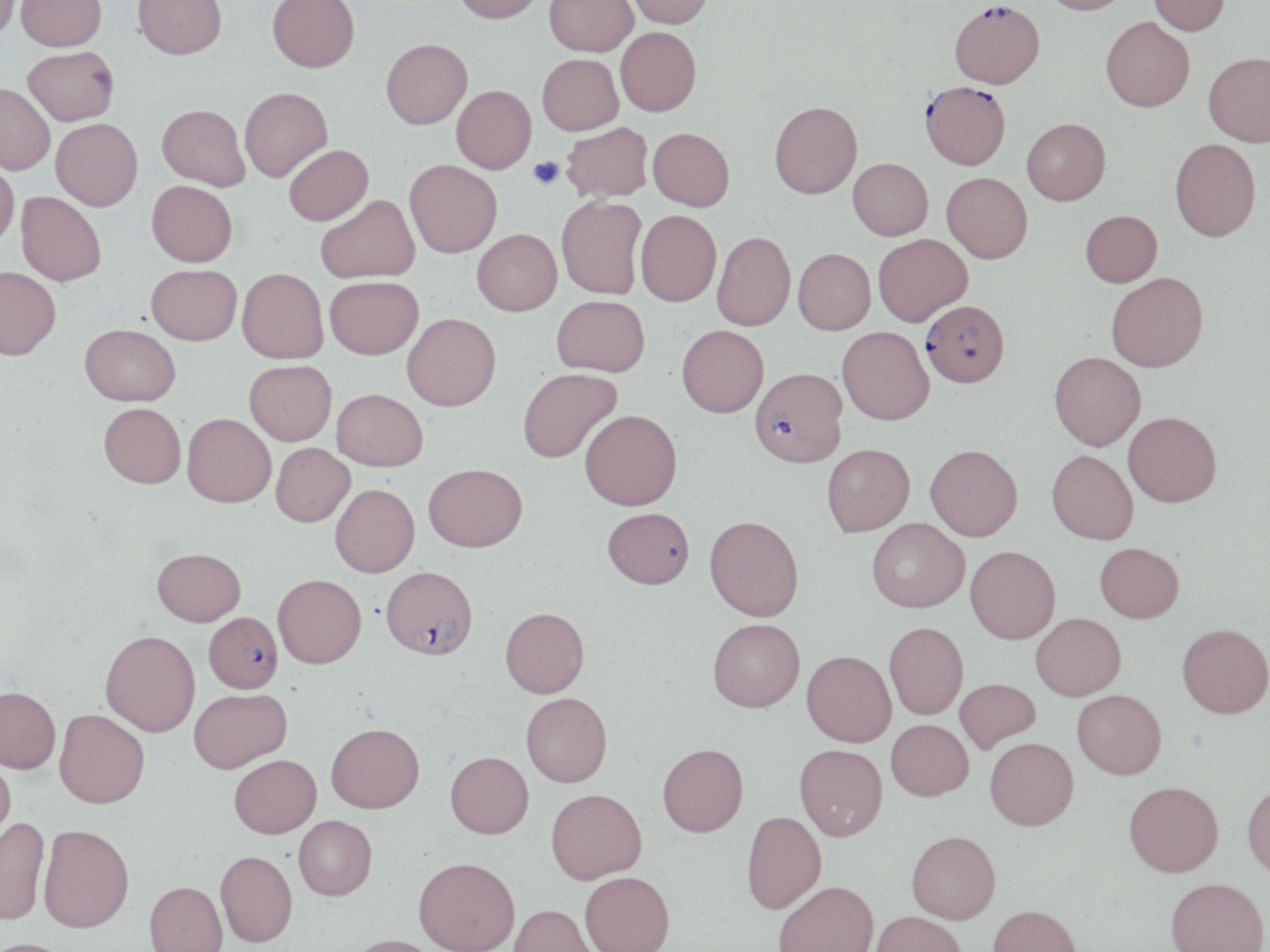
{
  "slide_level_diagnosis": "Plasmodium falciparum",
  "stain": "May-Grünwald-Giemsa",
  "magnification": "1000x",
  "platelet_locations": "approximate bounding boxes as [x1, y1, x2, y2] in pixels: [528, 156, 563, 189]",
  "preparation": "thin blood film",
  "uninfected_red_blood_cell_locations": "approximate bounding boxes as [x1, y1, x2, y2] in pixels: [15, 0, 108, 55], [133, 0, 227, 64], [266, 0, 359, 76], [455, 0, 544, 27], [545, 0, 638, 59], [625, 0, 712, 31], [1040, 0, 1132, 19], [1148, 0, 1230, 40], [0, 1, 21, 50], [1100, 21, 1194, 116], [616, 30, 701, 120], [381, 43, 472, 133], [23, 50, 118, 129], [1203, 56, 1269, 151], [538, 57, 623, 139], [0, 86, 53, 177], [452, 88, 537, 176], [240, 91, 332, 185], [769, 106, 863, 203], [156, 108, 249, 193], [51, 121, 143, 214], [1022, 122, 1111, 209], [562, 125, 653, 205], [647, 131, 734, 215], [1170, 142, 1261, 246], [285, 148, 374, 229], [847, 161, 933, 244], [0, 163, 19, 254], [405, 163, 502, 261], [941, 175, 1032, 267], [146, 184, 237, 270], [15, 194, 106, 289], [317, 197, 420, 285], [557, 198, 646, 301], [636, 213, 721, 310], [1081, 214, 1162, 290], [472, 232, 562, 320], [712, 234, 796, 334], [874, 236, 973, 329], [793, 252, 876, 338], [147, 267, 242, 349], [1, 270, 60, 363], [237, 271, 329, 366], [1106, 275, 1208, 375], [325, 280, 423, 363], [552, 298, 649, 379], [402, 316, 500, 414], [79, 327, 180, 409], [677, 328, 769, 421], [837, 329, 934, 428], [1050, 352, 1145, 451], [245, 362, 336, 447], [518, 369, 623, 464], [332, 390, 427, 471], [98, 404, 186, 490], [580, 411, 682, 511], [1123, 412, 1221, 506], [182, 414, 276, 508], [271, 443, 355, 527], [822, 444, 914, 535], [925, 444, 1023, 540], [1047, 450, 1138, 543], [423, 462, 527, 552], [330, 483, 419, 578], [603, 507, 694, 590], [704, 515, 804, 622], [866, 518, 969, 612], [1095, 542, 1184, 622], [965, 545, 1060, 643], [152, 549, 246, 626], [273, 574, 366, 668], [500, 607, 589, 697], [1031, 612, 1126, 699], [707, 618, 805, 712], [884, 622, 968, 719], [1177, 622, 1270, 718], [100, 630, 200, 736], [802, 650, 896, 746], [955, 678, 1040, 753], [0, 686, 61, 773], [188, 688, 292, 772], [1072, 689, 1166, 779], [520, 691, 612, 787], [54, 709, 149, 807], [886, 719, 973, 800], [326, 722, 424, 812], [985, 737, 1078, 829], [658, 743, 748, 836], [794, 743, 887, 840], [445, 751, 533, 837], [229, 754, 321, 838], [0, 756, 15, 846], [1124, 781, 1223, 876], [1242, 782, 1270, 877], [546, 788, 646, 883], [741, 810, 826, 913], [294, 815, 377, 900], [0, 817, 50, 925], [39, 823, 134, 932], [906, 830, 1000, 923], [215, 850, 297, 946], [414, 856, 520, 952], [580, 871, 674, 952], [1165, 877, 1269, 952], [773, 880, 878, 952], [145, 881, 227, 952], [509, 903, 597, 952], [988, 904, 1082, 952], [869, 911, 967, 952], [346, 934, 441, 952], [0, 938, 78, 952]",
  "field_of_view": "single",
  "modality": "optical microscopy",
  "plasmodium_falciparum_infected_red_blood_cell_locations": "approximate bounding boxes as [x1, y1, x2, y2] in pixels: [949, 6, 1044, 93], [919, 85, 1010, 174], [921, 304, 1009, 392], [749, 371, 847, 471], [381, 566, 478, 659], [204, 611, 283, 692]",
  "image_size": "1270×952 pixels"
}